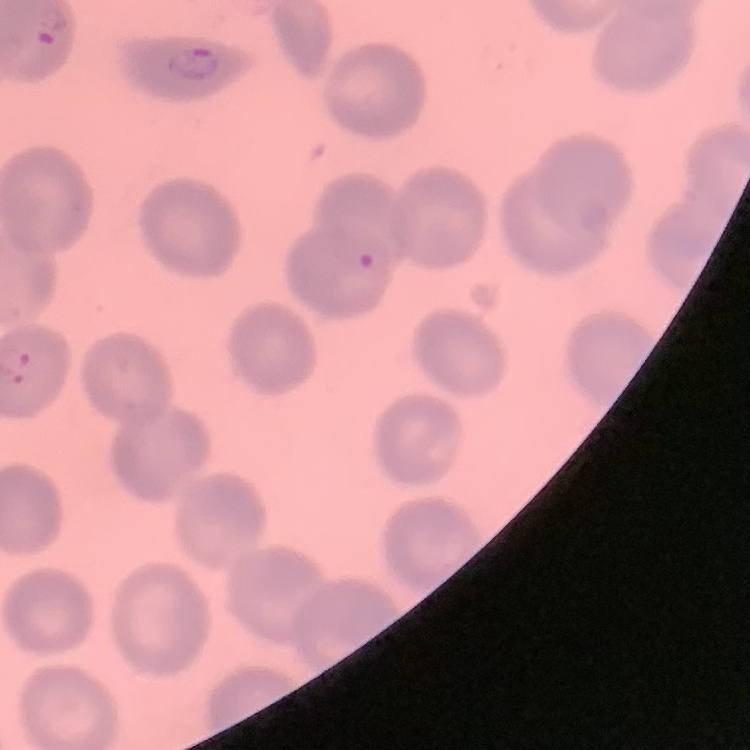
Summary:
  - Red blood cell morphology: no rouleaux formation
  - Image type: square crop of a larger photomicrograph
  - Stain: Field's or Giemsa
  - Preparation: thin blood film